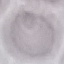
Summary:
  - Result: no malaria parasites detected
  - Stain: Giemsa
  - Capture: smartphone camera at the microscope eyepiece
  - Preparation: thin smear
  - Image type: automatically extracted cell patch, resized to 64 × 64 pixels